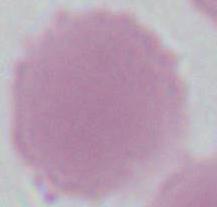

Summary:
  - Magnification: 1000x
  - Identification: red blood cell
  - Modality: micrograph